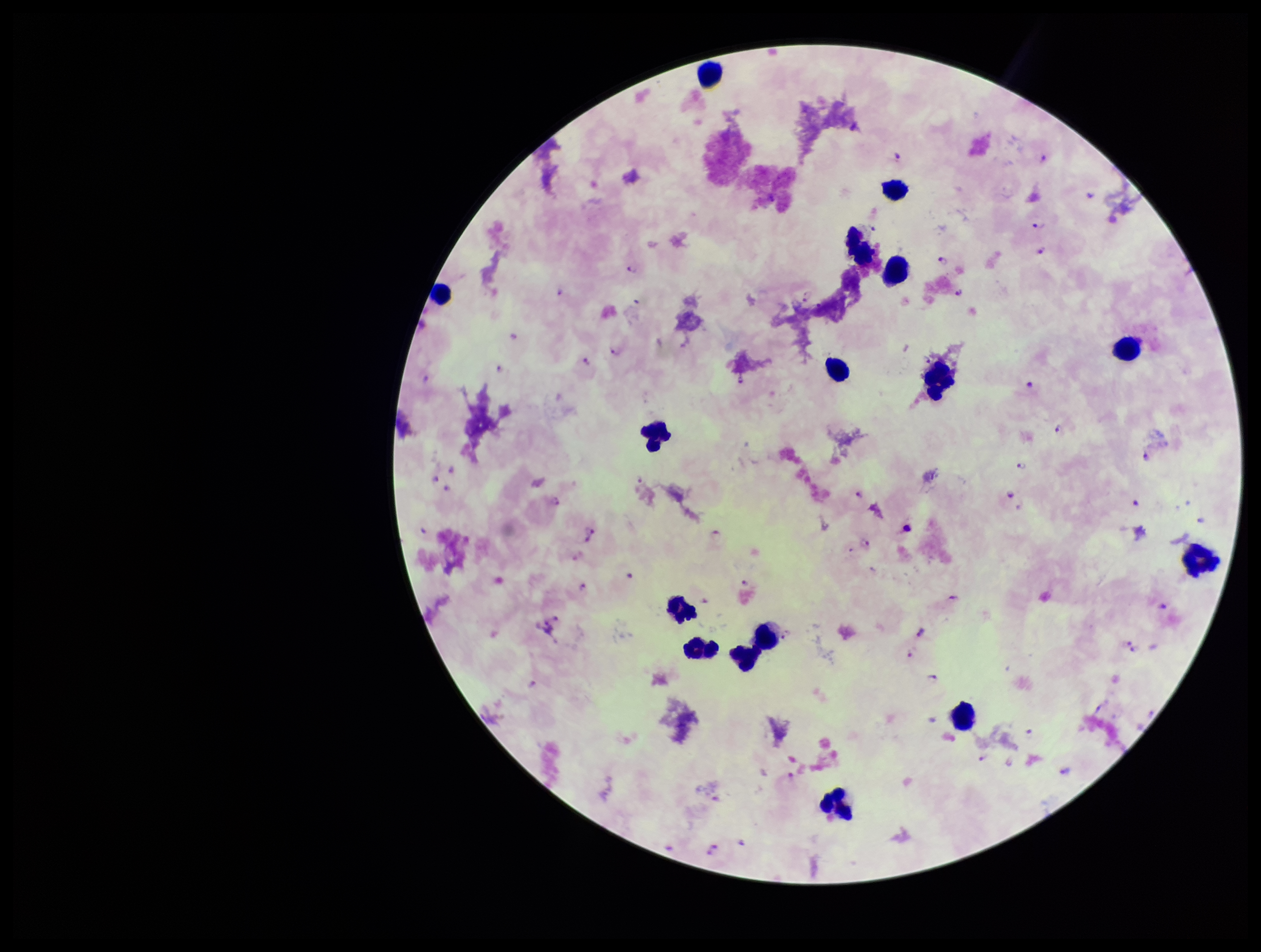

{
  "plasmodium_parasites": "identified",
  "leukocyte_count": 16,
  "capture": "smartphone photograph through the microscope eyepiece",
  "preparation": "thick",
  "image_size": "1261×952 pixels",
  "stain": "Giemsa",
  "parasite_count": 84,
  "field_of_view": "one from this slide",
  "patient_malaria_status": "positive",
  "species_reported_for_this_patient": "Plasmodium falciparum"
}